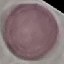 Result: no malaria parasites detected. Automatically extracted cell patch, resized to 64 × 64 pixels. Acquired by smartphone through the microscope eyepiece. Thin blood smear. Giemsa-stained preparation.